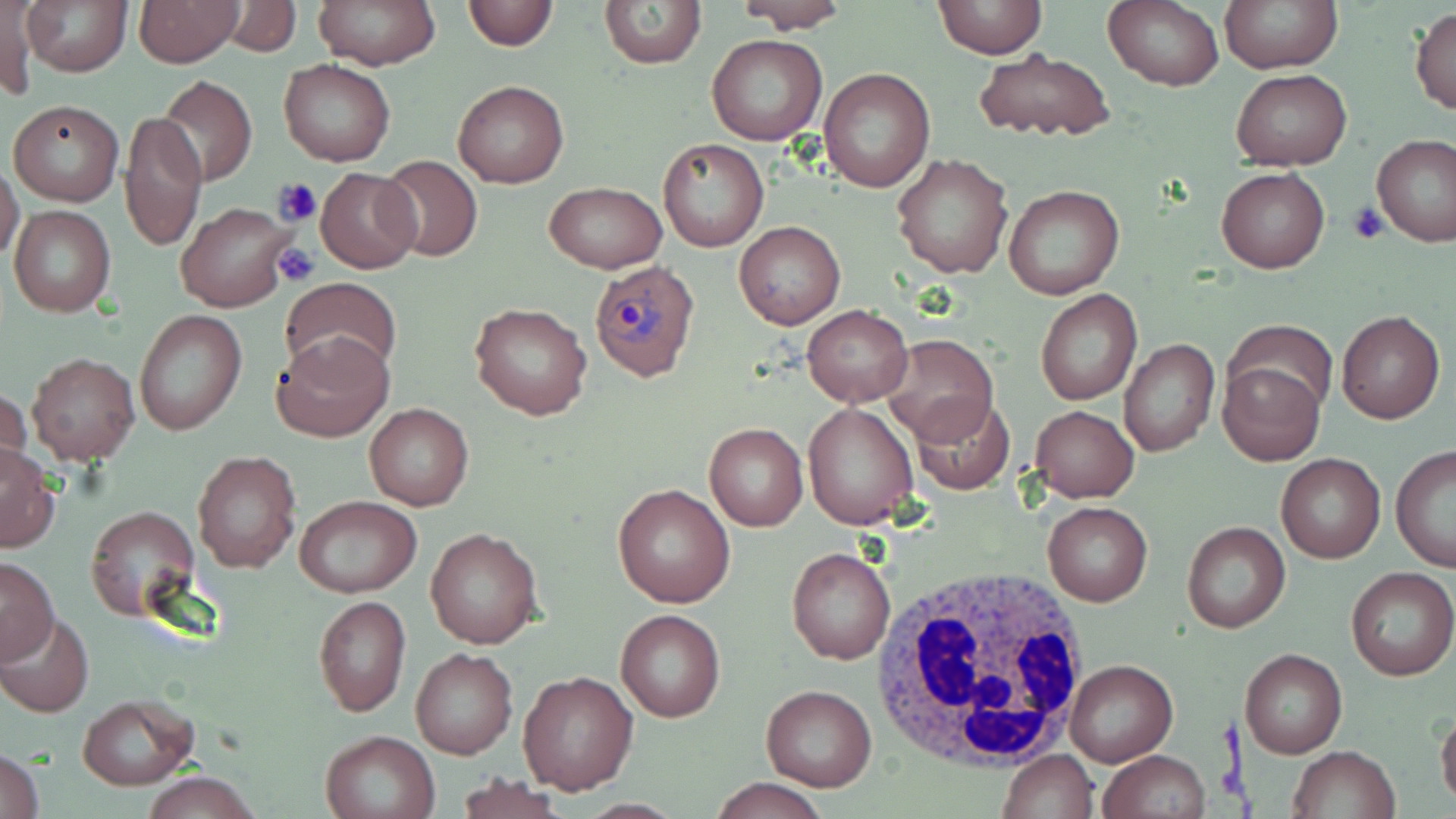

Summary:
  - Coordinate format: approximate bounding boxes as (x1, y1, x2, y2) in pixels
  - Plasmodium ovale-infected red blood cell locations: (589, 258, 701, 382)
  - White blood cell locations: (873, 566, 1092, 771)
  - Platelet locations: (274, 178, 322, 226), (1348, 201, 1389, 245), (274, 243, 320, 287)
  - Uninfected red blood cell locations: (21, 0, 132, 76), (132, 0, 244, 67), (315, 0, 442, 69), (463, 0, 556, 52), (598, 0, 705, 69), (1220, 0, 1341, 72), (1, 1, 39, 103), (931, 1, 1048, 59), (221, 2, 299, 55), (729, 2, 853, 31), (1103, 2, 1223, 91), (1411, 7, 1456, 114), (707, 35, 827, 146), (973, 48, 1115, 143), (278, 59, 395, 166), (819, 66, 936, 194), (1233, 69, 1351, 169), (157, 75, 257, 187), (453, 79, 569, 188), (7, 100, 123, 205), (121, 107, 207, 253), (1371, 132, 1456, 247), (659, 138, 768, 252), (892, 153, 1013, 280), (376, 156, 483, 262), (0, 162, 24, 262), (315, 168, 421, 273), (1216, 168, 1329, 274), (541, 181, 667, 273), (1002, 183, 1125, 299), (178, 202, 294, 311), (9, 205, 116, 316), (734, 219, 846, 331), (279, 276, 401, 384), (1035, 288, 1142, 407), (471, 302, 592, 420), (802, 304, 912, 406), (133, 309, 247, 438), (1336, 310, 1445, 424), (1228, 323, 1332, 422), (272, 332, 395, 443), (880, 333, 999, 446), (1119, 338, 1220, 458), (27, 352, 139, 465), (1220, 362, 1325, 465), (0, 386, 32, 485), (912, 395, 1014, 494), (802, 401, 920, 530), (364, 402, 475, 511), (1029, 405, 1140, 501), (703, 423, 808, 531), (0, 444, 61, 552), (1390, 448, 1456, 573), (192, 451, 300, 573), (1276, 454, 1385, 563), (612, 482, 736, 608), (293, 495, 421, 598), (1042, 501, 1153, 606), (84, 505, 199, 620), (1182, 520, 1290, 634), (424, 527, 544, 648), (786, 545, 896, 666), (0, 558, 58, 664), (1345, 568, 1456, 681), (312, 595, 410, 717), (615, 608, 726, 722), (1, 612, 94, 716), (410, 647, 519, 761), (1240, 648, 1347, 758), (1065, 658, 1178, 767), (517, 671, 638, 795), (760, 684, 878, 791), (75, 694, 199, 790), (1436, 708, 1456, 808), (320, 730, 440, 819), (1, 746, 45, 819), (1286, 746, 1399, 819), (997, 749, 1099, 819), (1099, 750, 1210, 819), (139, 772, 263, 818), (454, 773, 567, 819), (706, 778, 831, 817)
  - Slide-level diagnosis: Plasmodium ovale
  - Modality: optical microscopy
  - Preparation: thin blood smear
  - Image size: 1456×819 pixels
  - Magnification: 1000x
  - Stain: May-Grünwald-Giemsa
  - Field of view: one of a larger specimen